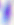
modality = micrograph
magnification = 400x
identification = Toxoplasma gondii